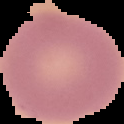
preparation = thin blood smear
image size = 124×124 pixels
image type = cell region segmented out of the field of view; surrounding area masked to black
malaria status = uninfected